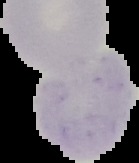
Malaria status: uninfected. Image is 139×163 pixels. Segmented cell region on a black background. From a thin blood film.